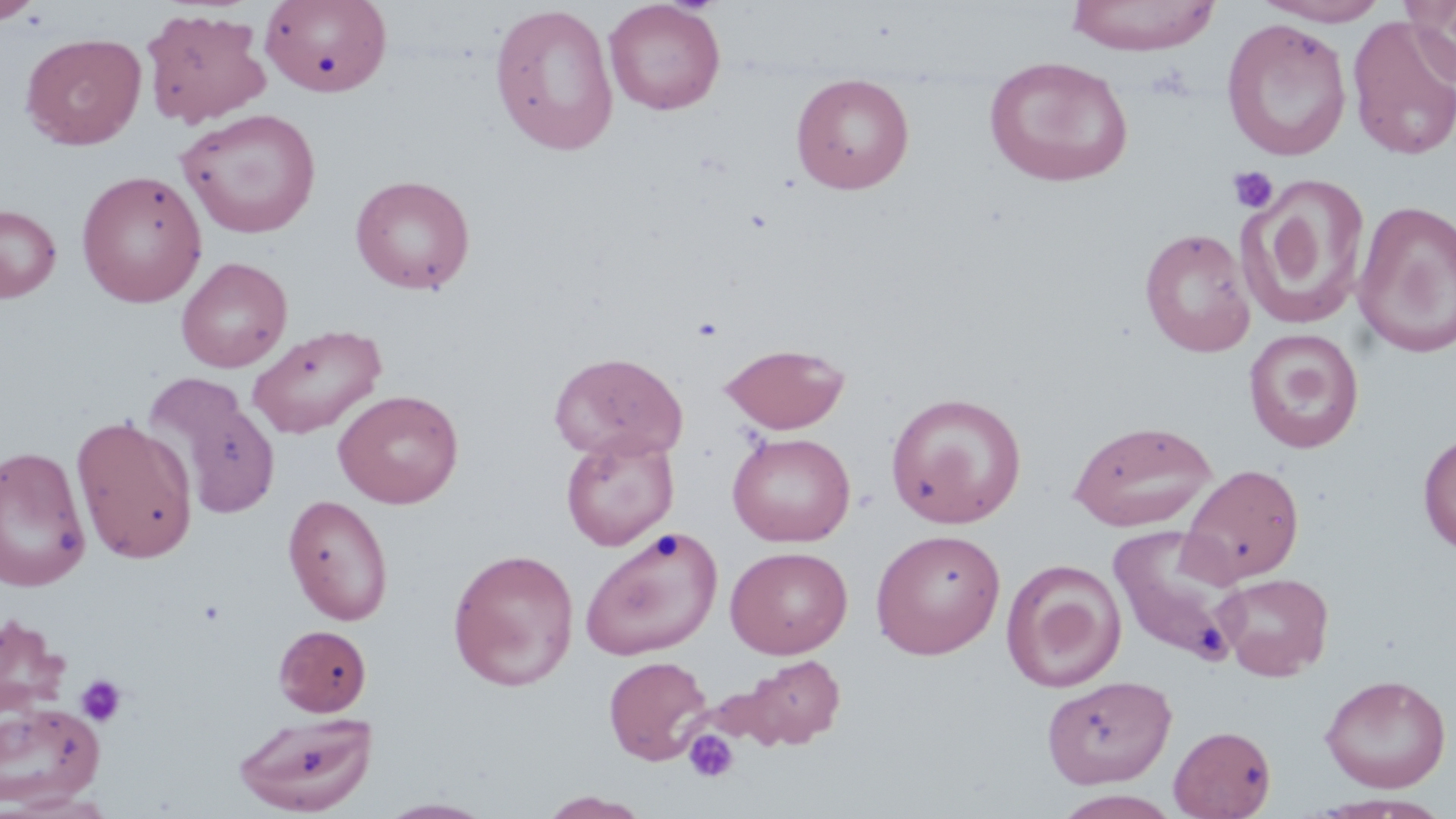

slide-level diagnosis = negative for blood parasites
field of view = one of a larger specimen
modality = optical microscopy
uninfected red blood cell locations = approximate bounding boxes as [x1, y1, x2, y2] in pixels: [0, 0, 44, 25], [604, 0, 727, 115], [1064, 0, 1222, 55], [260, 1, 393, 98], [1252, 1, 1390, 26], [1402, 1, 1456, 88], [488, 3, 619, 157], [141, 7, 272, 128], [1347, 16, 1456, 161], [1221, 17, 1352, 162], [21, 32, 146, 150], [984, 56, 1134, 187], [790, 73, 915, 194], [177, 108, 322, 238], [76, 169, 208, 307], [350, 174, 475, 295], [1237, 175, 1371, 332], [1353, 199, 1456, 358], [0, 204, 62, 301], [1139, 227, 1256, 357], [176, 256, 293, 373], [247, 322, 387, 439], [1243, 328, 1365, 453], [719, 342, 850, 434], [549, 351, 687, 462], [141, 372, 282, 523], [333, 389, 464, 508], [886, 392, 1028, 528], [70, 414, 199, 564], [1068, 420, 1217, 532], [560, 431, 679, 551], [727, 432, 856, 547], [1417, 432, 1456, 556], [0, 445, 92, 592], [1179, 463, 1305, 586], [282, 494, 394, 625], [1107, 524, 1249, 667], [580, 527, 723, 659], [871, 528, 1006, 658], [725, 546, 853, 658], [447, 548, 580, 691], [1001, 559, 1126, 692], [1216, 572, 1334, 681], [0, 614, 72, 717], [272, 625, 371, 717], [602, 655, 713, 765], [735, 655, 846, 750], [1319, 673, 1451, 793], [1042, 675, 1177, 789], [0, 701, 105, 808], [233, 711, 377, 816], [1169, 724, 1277, 819], [3, 790, 116, 818], [540, 790, 652, 818], [376, 799, 497, 818]
platelet locations = approximate bounding boxes as [x1, y1, x2, y2] in pixels: [1227, 166, 1279, 214], [691, 316, 724, 341], [75, 674, 128, 727], [683, 729, 739, 783]
stain = May-Grünwald-Giemsa
image size = 1456×819 pixels
magnification = 1000x
preparation = thin blood film